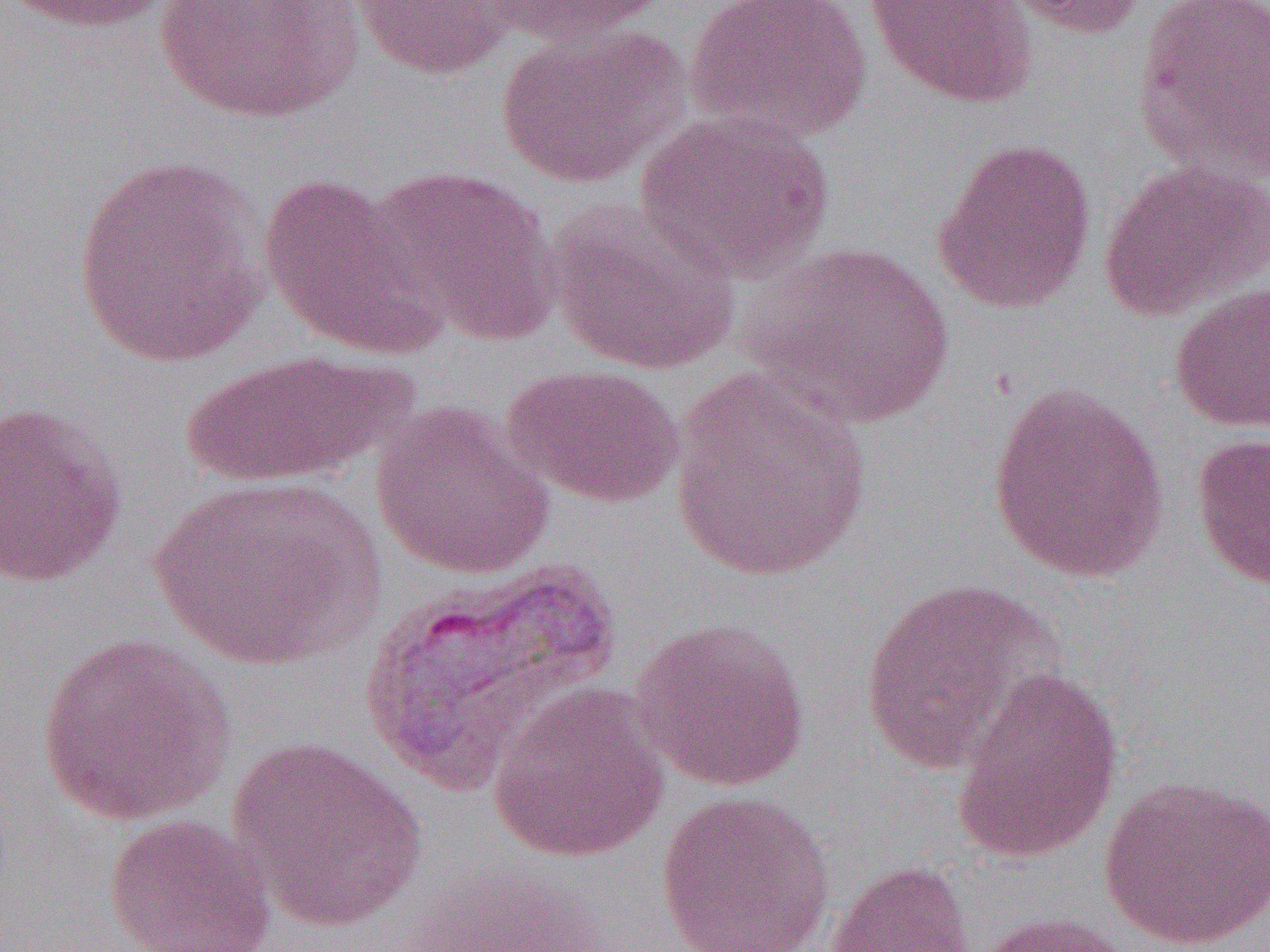
Summary:
  - Coordinate format: approximate bounding boxes as (x1,y1)-(x2,y2) corner pairs in pixels
  - Uninfected red blood cell locations: (8,0)-(174,34), (347,0)-(518,80), (478,0)-(671,48), (687,0)-(874,143), (863,0)-(1039,110), (997,0)-(1151,39), (1131,0)-(1270,181), (152,1)-(364,123), (494,22)-(691,190), (635,110)-(835,284), (932,137)-(1097,315), (71,154)-(269,369), (1100,160)-(1268,321), (364,165)-(561,346), (258,173)-(440,355), (547,200)-(739,376), (745,241)-(955,429), (1168,279)-(1270,433), (179,349)-(414,489), (503,363)-(685,508), (666,371)-(874,583), (987,381)-(1170,582), (0,400)-(127,588), (369,402)-(555,580), (1190,432)-(1270,592), (147,474)-(385,670), (357,561)-(624,792), (858,578)-(1057,773), (630,617)-(812,792), (35,632)-(236,827), (951,666)-(1124,865), (487,682)-(669,863), (226,737)-(427,930), (1098,774)-(1270,951), (655,789)-(836,952), (102,813)-(277,952), (823,860)-(977,952), (975,911)-(1142,952)
  - Slide-level diagnosis: Plasmodium vivax
  - Field of view: one of a larger specimen
  - Preparation: thin blood smear
  - Modality: light microscopy
  - Image size: 1270×952 pixels
  - Magnification: 1000x